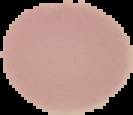

image type = segmented cell region on a black background
preparation = thin blood smear
malaria status = uninfected
image size = 133×115 pixels